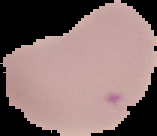

image size = 157×136 pixels
malaria status = uninfected
preparation = thin blood film
image type = cell region segmented out of the field of view; surrounding area masked to black